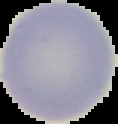
preparation = thin blood film
image size = 118×124 pixels
image type = cell region segmented out of the field of view; surrounding area masked to black
malaria status = uninfected